Assess this cell for malaria.
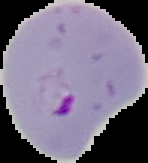
Parasitized.

Summary:
  - Image size: 148×163 pixels
  - Image type: segmented cell region on a black background
  - Preparation: thin blood smear